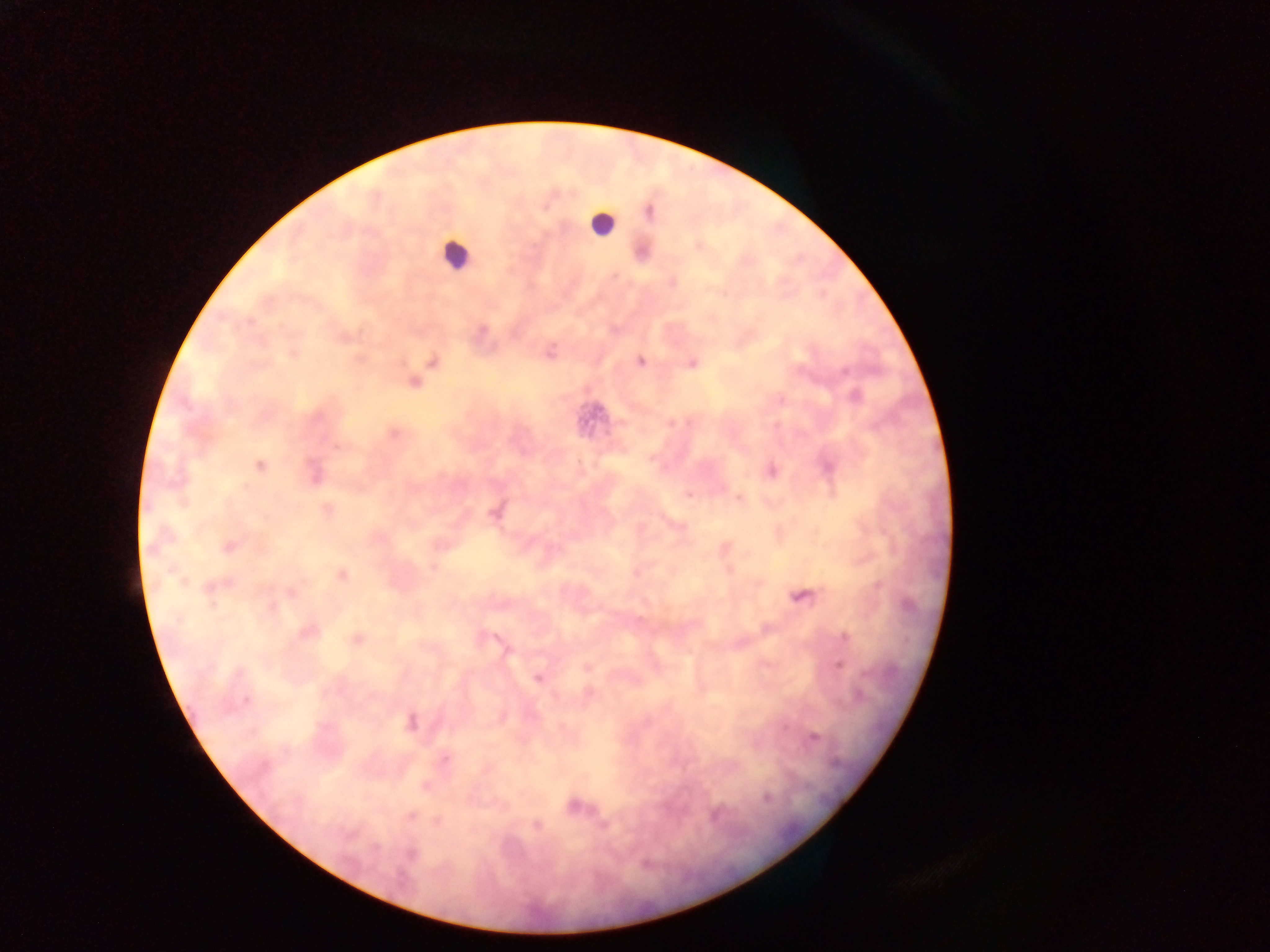

Approximate centers as [x, y] in pixels. Plasmodium parasite locations: [545, 207], [649, 212], [550, 352], [432, 361], [640, 361], [692, 364], [844, 372], [414, 382], [855, 396], [393, 433], [259, 466], [773, 472], [689, 494], [327, 509], [495, 513], [229, 546], [343, 575], [213, 588], [291, 593], [803, 597], [305, 632], [845, 637], [358, 640], [838, 665], [587, 668], [538, 678], [246, 700], [411, 723], [815, 738], [445, 759], [425, 786], [766, 798], [574, 806], [411, 817], [438, 821], [537, 825], [604, 826], [410, 854]. Leukocyte locations: [600, 225], [455, 252]. Mobile-phone photograph taken through the microscope. Thick blood smear. Single field of view. Collected in Ghana. Image is 1270×952 pixels.